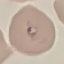
malaria status = parasitized
capture = smartphone camera at the microscope eyepiece
preparation = thin blood smear
stain = Giemsa
image type = cell patch, automatically extracted from a larger field of view and resized to 64 × 64 pixels